State the blood parasite species.
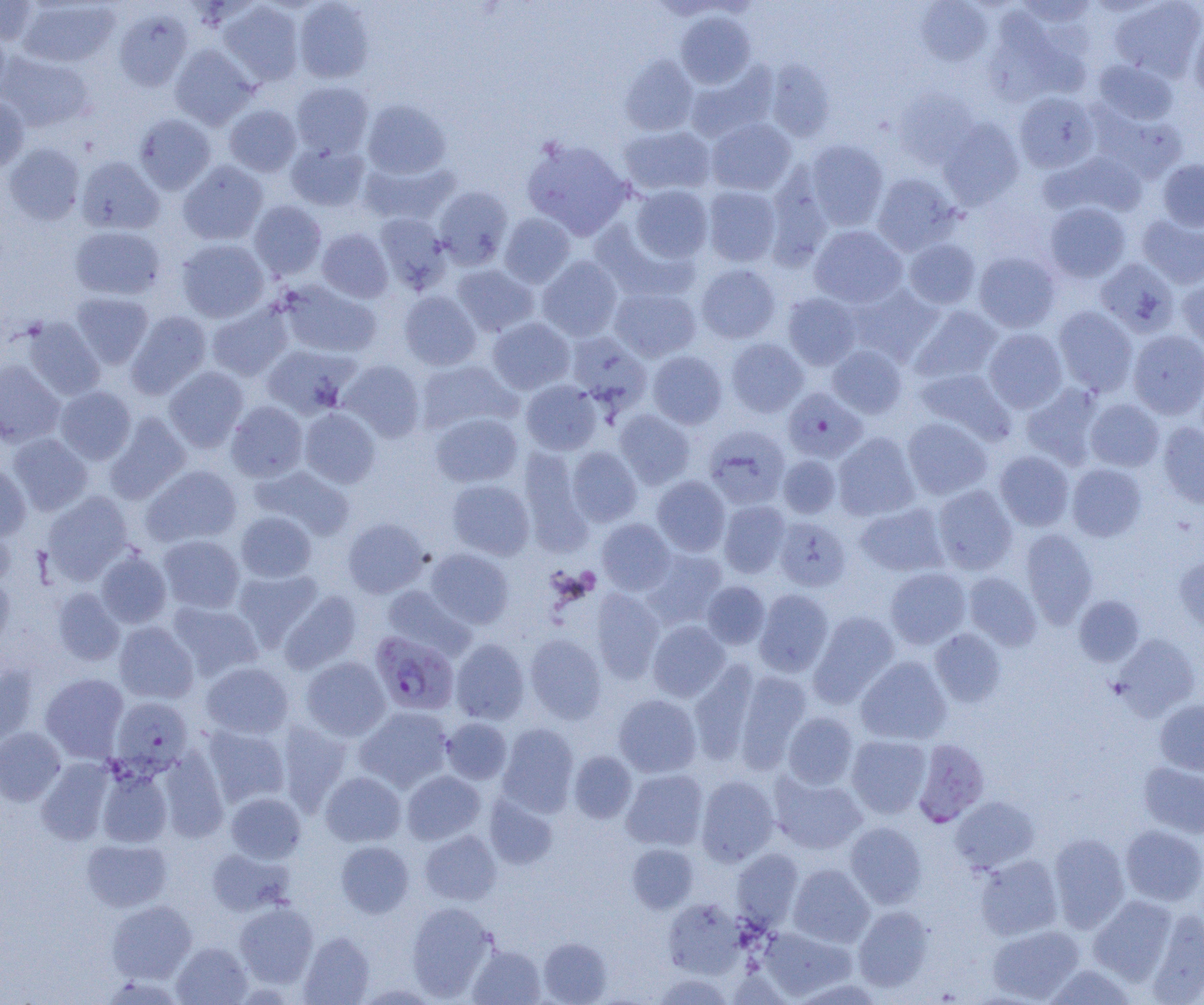

Plasmodium falciparum.

Approximate bounding boxes as (x1, y1, x2, y2) in pixels. Uninfected red blood cell locations (subset): (0, 0, 40, 45), (17, 0, 120, 68), (293, 0, 375, 83), (1015, 0, 1096, 27), (218, 1, 304, 86), (915, 1, 992, 66), (1110, 1, 1204, 81), (114, 9, 193, 91), (675, 11, 756, 88), (983, 15, 1077, 106), (1189, 21, 1204, 100), (0, 25, 10, 101), (170, 44, 258, 129), (0, 52, 94, 132), (620, 55, 698, 136), (1093, 59, 1178, 125), (765, 60, 835, 141), (685, 62, 777, 143), (291, 81, 374, 158), (894, 87, 978, 168), (1014, 92, 1099, 173), (0, 95, 30, 172), (362, 99, 451, 179), (224, 104, 301, 176), (134, 114, 216, 194), (706, 117, 797, 195), (938, 118, 1024, 209), (619, 125, 716, 196), (522, 136, 633, 240), (804, 139, 889, 230), (3, 142, 85, 225), (287, 142, 369, 211), (1042, 151, 1147, 220), (76, 156, 164, 235), (361, 158, 459, 225), (1158, 159, 1204, 231), (177, 160, 268, 245), (871, 173, 960, 255), (630, 185, 713, 263), (434, 186, 513, 269), (702, 186, 781, 267), (249, 200, 327, 279), (1044, 202, 1131, 282), (499, 212, 575, 288), (375, 213, 451, 294), (1136, 214, 1204, 289), (592, 219, 699, 303), (69, 225, 165, 300), (809, 225, 908, 308), (317, 228, 393, 303), (904, 238, 981, 309), (176, 239, 269, 322), (974, 251, 1061, 333), (537, 256, 622, 341), (1095, 258, 1180, 337), (696, 263, 781, 344), (452, 264, 539, 336), (1177, 278, 1204, 354), (278, 280, 381, 358), (846, 284, 943, 366), (610, 286, 701, 362), (399, 290, 482, 370), (69, 292, 153, 368), (783, 293, 861, 370), (206, 301, 293, 381), (909, 305, 1003, 385), (1054, 306, 1138, 396), (126, 311, 211, 399), (22, 317, 105, 400), (487, 317, 575, 394), (984, 328, 1067, 412), (1128, 330, 1204, 419), (565, 332, 651, 415), (726, 338, 809, 417), (261, 344, 357, 419), (827, 344, 907, 418), (648, 350, 727, 429), (0, 360, 65, 447), (338, 360, 425, 442), (415, 360, 520, 435), (164, 366, 249, 452), (914, 368, 1015, 445), (521, 380, 601, 454), (1020, 383, 1105, 469), (55, 386, 136, 464), (1085, 399, 1164, 471), (226, 401, 308, 482), (299, 407, 380, 488), (614, 409, 695, 489), (104, 412, 190, 504), (431, 413, 522, 487), (902, 417, 992, 500), (1158, 422, 1204, 508), (704, 426, 790, 510), (833, 432, 920, 521), (8, 433, 93, 515), (567, 446, 642, 527), (518, 447, 593, 553), (994, 450, 1074, 530), (778, 455, 841, 519), (0, 462, 31, 542), (1067, 463, 1147, 541), (141, 464, 242, 547), (250, 465, 355, 540), (652, 476, 730, 556), (447, 479, 534, 560), (933, 485, 1017, 575), (42, 492, 133, 583), (719, 500, 790, 578), (855, 502, 949, 577), (236, 511, 317, 583), (773, 515, 851, 592), (342, 517, 429, 598), (597, 518, 675, 595), (0, 522, 15, 589), (1020, 528, 1097, 627), (158, 534, 245, 613), (424, 548, 514, 629), (642, 548, 728, 627), (96, 550, 172, 628), (1174, 556, 1204, 635), (885, 567, 971, 648), (232, 568, 323, 649), (964, 572, 1041, 651), (0, 576, 15, 654), (702, 581, 770, 649), (382, 585, 474, 660), (52, 588, 125, 666), (590, 589, 664, 683), (754, 589, 834, 676), (278, 590, 361, 673), (1074, 595, 1145, 666), (167, 601, 263, 680), (809, 611, 900, 707), (648, 620, 730, 702), (114, 622, 198, 704), (930, 629, 1005, 707), (1112, 633, 1201, 719), (525, 634, 606, 724), (451, 638, 530, 725), (300, 656, 390, 740), (856, 656, 952, 745), (200, 661, 293, 739), (689, 661, 761, 766), (0, 665, 38, 746), (733, 669, 812, 772), (40, 673, 129, 762), (614, 694, 701, 777), (1155, 699, 1204, 776), (355, 706, 453, 792), (782, 712, 858, 789), (441, 717, 512, 784), (276, 721, 353, 813), (498, 723, 579, 816), (202, 724, 290, 807), (0, 728, 65, 806), (846, 735, 931, 818), (157, 750, 229, 842), (568, 751, 637, 824), (36, 758, 115, 845), (1139, 762, 1204, 838), (97, 768, 172, 848), (621, 769, 708, 850), (401, 770, 485, 844), (320, 771, 406, 846), (770, 772, 867, 854), (696, 775, 779, 865), (226, 792, 306, 863), (484, 794, 558, 870), (951, 796, 1039, 873), (845, 821, 927, 908), (1120, 825, 1204, 906), (419, 830, 501, 905), (1048, 833, 1130, 932), (81, 837, 172, 911), (335, 841, 414, 918), (627, 843, 698, 913), (207, 847, 294, 916), (731, 849, 803, 929), (975, 854, 1063, 940), (788, 864, 874, 947), (1088, 895, 1179, 985), (662, 898, 744, 979), (106, 900, 196, 983), (234, 902, 318, 987), (406, 902, 495, 1000), (853, 906, 933, 992), (1145, 909, 1204, 1002), (987, 924, 1084, 1002), (759, 927, 854, 1000), (298, 932, 375, 1005), (538, 937, 612, 1004), (171, 942, 252, 1004), (467, 944, 546, 1005), (1042, 963, 1136, 1004), (653, 973, 733, 1005). Plasmodium falciparum-infected red blood cell locations (subset): (783, 388, 867, 463), (369, 631, 459, 716), (110, 697, 193, 776). Optical microscopy. Captured at 1000x magnification. One field of a larger specimen. Image is 1204×1005 pixels. Thin blood film.